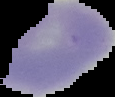 The area outside the segmented cell region is set to black. From a thin blood film. Image is 115×97 pixels. Result: no malaria parasites detected.